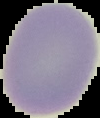

Image is 100×118 pixels. Segmented cell region on a black background. Malaria status: uninfected. From a thin blood smear.